Locate and identify every blood parasite.
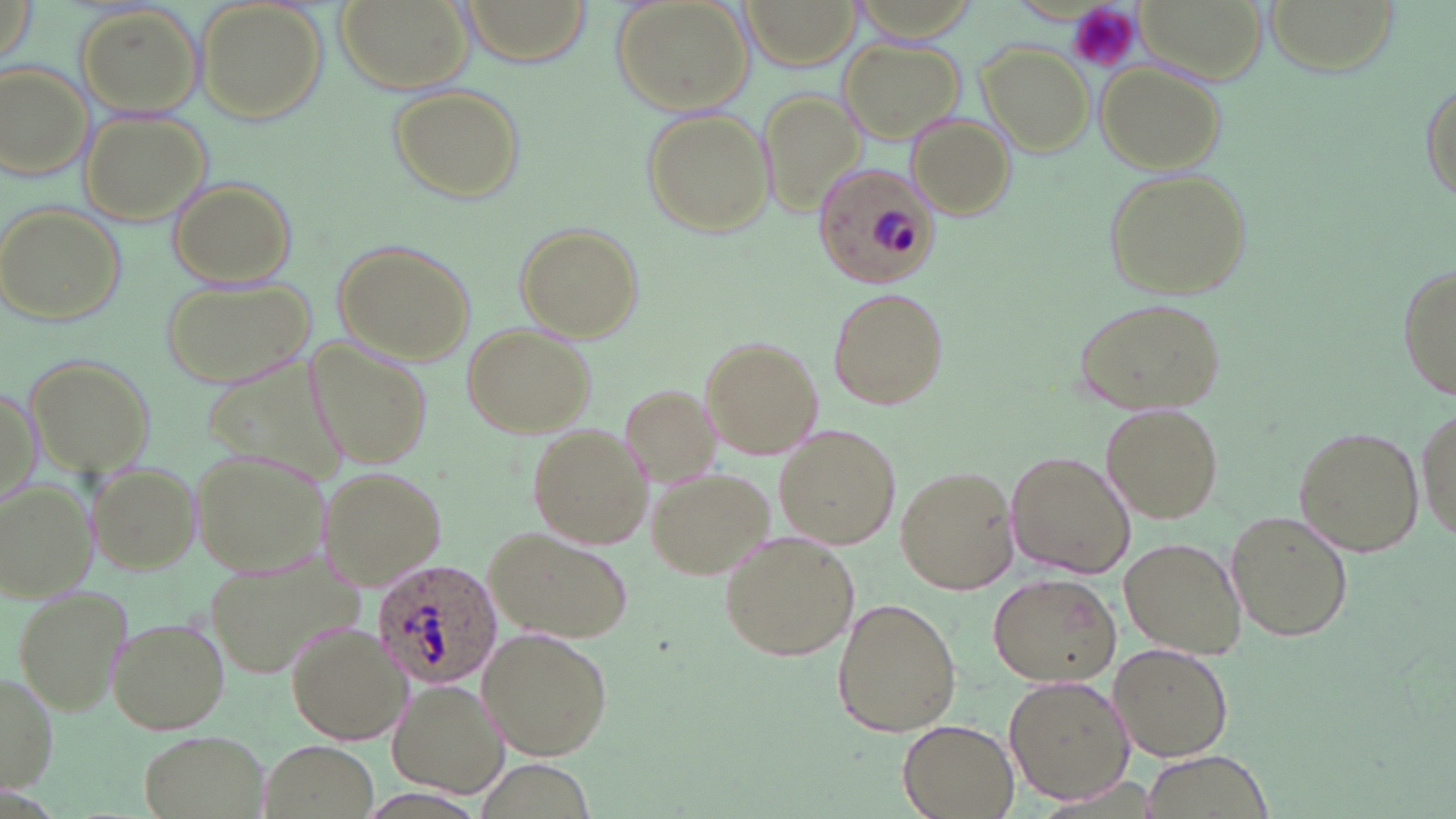

Approximate bounding boxes as named x1/y1/x2/y2 corners in pixels.
Plasmodium ovale-infected red blood cells: (x1=816, y1=164, x2=944, y2=287), (x1=371, y1=557, x2=502, y2=689).
No Plasmodium falciparum, Plasmodium malariae, Plasmodium vivax, Babesia divergens, or Trypanosoma brucei observed.

Summary:
  - Platelet locations: (x1=1068, y1=2, x2=1141, y2=73)
  - Uninfected red blood cell locations: (x1=198, y1=0, x2=329, y2=125), (x1=334, y1=0, x2=477, y2=98), (x1=458, y1=0, x2=590, y2=63), (x1=612, y1=0, x2=752, y2=112), (x1=741, y1=0, x2=858, y2=71), (x1=1262, y1=0, x2=1398, y2=73), (x1=1, y1=1, x2=38, y2=75), (x1=75, y1=4, x2=205, y2=117), (x1=840, y1=39, x2=966, y2=143), (x1=978, y1=41, x2=1095, y2=155), (x1=1097, y1=60, x2=1228, y2=175), (x1=2, y1=62, x2=94, y2=184), (x1=1417, y1=75, x2=1454, y2=203), (x1=388, y1=83, x2=525, y2=201), (x1=760, y1=88, x2=866, y2=218), (x1=640, y1=108, x2=773, y2=237), (x1=79, y1=111, x2=211, y2=227), (x1=906, y1=113, x2=1014, y2=220), (x1=1101, y1=165, x2=1252, y2=301), (x1=168, y1=176, x2=297, y2=291), (x1=2, y1=206, x2=124, y2=326), (x1=514, y1=223, x2=643, y2=337), (x1=331, y1=238, x2=477, y2=364), (x1=1396, y1=265, x2=1455, y2=399), (x1=160, y1=275, x2=314, y2=388), (x1=825, y1=286, x2=950, y2=410), (x1=1072, y1=295, x2=1227, y2=417), (x1=460, y1=323, x2=595, y2=439), (x1=702, y1=336, x2=824, y2=461), (x1=308, y1=338, x2=435, y2=474), (x1=23, y1=352, x2=155, y2=479), (x1=199, y1=352, x2=349, y2=490), (x1=1, y1=382, x2=41, y2=513), (x1=619, y1=382, x2=724, y2=486), (x1=1100, y1=403, x2=1224, y2=523), (x1=1415, y1=403, x2=1454, y2=545), (x1=526, y1=420, x2=653, y2=549), (x1=1293, y1=425, x2=1424, y2=557), (x1=777, y1=426, x2=900, y2=549), (x1=194, y1=449, x2=334, y2=575), (x1=1004, y1=451, x2=1136, y2=579), (x1=88, y1=461, x2=202, y2=573), (x1=319, y1=465, x2=444, y2=591), (x1=895, y1=465, x2=1018, y2=596), (x1=649, y1=470, x2=772, y2=582), (x1=0, y1=480, x2=96, y2=599), (x1=1224, y1=508, x2=1353, y2=644), (x1=484, y1=529, x2=633, y2=642), (x1=719, y1=529, x2=859, y2=662), (x1=1119, y1=537, x2=1246, y2=661), (x1=203, y1=559, x2=362, y2=678), (x1=988, y1=573, x2=1121, y2=686), (x1=12, y1=582, x2=132, y2=718), (x1=831, y1=597, x2=962, y2=738), (x1=108, y1=614, x2=230, y2=734), (x1=286, y1=622, x2=409, y2=745), (x1=476, y1=628, x2=613, y2=760), (x1=1108, y1=641, x2=1234, y2=762), (x1=1, y1=671, x2=59, y2=791), (x1=1005, y1=676, x2=1132, y2=805), (x1=388, y1=677, x2=509, y2=798), (x1=896, y1=718, x2=1020, y2=819), (x1=139, y1=729, x2=269, y2=819), (x1=264, y1=738, x2=376, y2=819), (x1=1139, y1=752, x2=1278, y2=819)
  - Slide-level diagnosis: Plasmodium ovale
  - Magnification: 1000x
  - Image size: 1456×819 pixels
  - Preparation: thin blood smear
  - Modality: light microscopy
  - Field of view: one of a larger specimen
  - Stain: May-Grünwald-Giemsa